Point out each leukocyte.
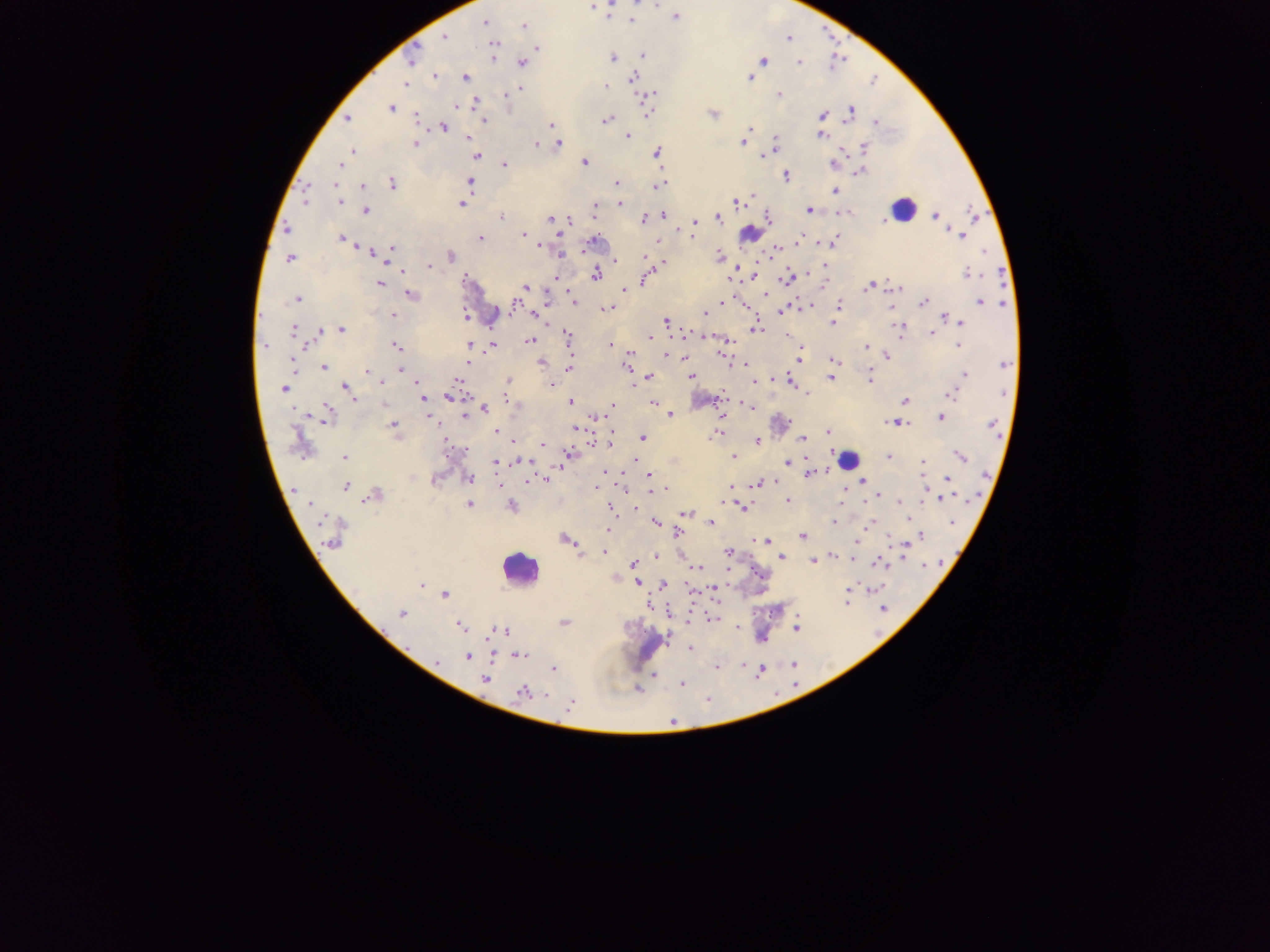

Approximate centers as (x, y) in pixels.
Leukocytes: (901, 210), (750, 233), (848, 460), (519, 568).

Summary:
  - Malaria parasite locations: (592, 5), (607, 15), (675, 16), (631, 19), (484, 22), (523, 26), (444, 37), (788, 37), (493, 44), (536, 49), (642, 55), (493, 58), (613, 58), (411, 59), (764, 60), (520, 62), (799, 62), (433, 76), (465, 76), (749, 77), (631, 79), (406, 83), (605, 86), (520, 89), (505, 93), (652, 93), (778, 93), (475, 99), (455, 106), (390, 107), (850, 110), (648, 113), (713, 113), (821, 116), (347, 118), (417, 118), (607, 119), (483, 120), (875, 122), (550, 125), (442, 126), (750, 128), (821, 135), (745, 136), (467, 137), (628, 137), (774, 140), (741, 142), (415, 143), (557, 143), (535, 144), (863, 148), (775, 149), (352, 150), (657, 153), (476, 156), (584, 161), (340, 164), (504, 164), (858, 172), (786, 175), (470, 181), (391, 182), (617, 184), (658, 184), (361, 186), (336, 188), (305, 190), (835, 190), (751, 194), (305, 198), (734, 200), (339, 201), (462, 203), (620, 204), (594, 208), (810, 209), (366, 210), (840, 211), (663, 215), (934, 215), (500, 216), (551, 218), (717, 218), (767, 218), (881, 218), (643, 219), (694, 222), (286, 228), (693, 230), (523, 234), (961, 235), (342, 238), (479, 238), (799, 239), (592, 241), (657, 241), (835, 241), (538, 246), (391, 247), (581, 250), (776, 250), (370, 251), (389, 253), (451, 255), (559, 255), (382, 256), (718, 256), (289, 258), (645, 258), (615, 259), (662, 262), (429, 265), (736, 266), (824, 266), (400, 271), (595, 273), (966, 274), (754, 276), (465, 278), (787, 278), (643, 280), (729, 281), (380, 283), (867, 286), (526, 287), (899, 288), (622, 289), (565, 290), (410, 295), (765, 295), (570, 296), (296, 299), (739, 300), (721, 302), (923, 302), (980, 302), (1002, 302), (573, 304), (743, 305), (838, 305), (891, 305), (512, 306), (802, 306), (810, 306), (606, 308), (782, 312), (702, 314), (392, 315), (467, 315), (535, 315), (462, 316), (943, 316), (834, 320), (665, 321), (960, 322), (832, 323), (753, 327), (898, 329), (294, 330), (340, 330), (319, 331), (931, 332), (686, 333), (567, 335), (648, 337), (726, 339), (531, 340), (470, 344), (475, 344), (610, 344), (956, 344), (492, 345), (263, 346), (395, 346), (866, 346), (798, 350), (629, 353), (722, 353), (665, 355), (886, 355), (684, 358), (798, 359), (832, 360), (291, 362), (466, 362), (541, 362), (744, 364), (323, 367), (401, 368), (569, 368), (367, 370), (964, 375), (649, 377), (691, 377), (830, 377), (773, 378), (868, 378), (457, 380), (508, 380), (790, 381), (382, 382), (632, 382), (752, 382), (416, 384), (506, 384), (551, 384), (346, 387), (284, 389), (805, 392), (950, 395), (451, 397), (352, 399), (427, 399), (719, 400), (904, 400), (424, 402), (570, 402), (742, 402), (385, 403), (654, 403), (746, 405), (612, 407), (484, 408), (326, 414), (671, 414), (428, 415), (464, 416), (597, 416), (941, 418), (890, 422), (899, 423), (392, 425), (575, 428), (495, 431), (828, 431), (714, 435), (805, 437), (642, 439), (444, 440), (803, 440), (512, 441), (610, 441), (591, 442), (755, 442), (299, 443), (543, 444), (462, 452), (888, 456), (960, 456), (345, 457), (733, 457), (565, 458), (636, 459), (520, 460), (787, 461), (496, 462), (922, 463), (606, 471), (809, 473), (648, 474), (467, 478), (856, 478), (947, 478), (862, 479), (435, 480), (545, 480), (648, 481), (774, 481), (757, 484), (344, 485), (498, 485), (731, 486), (844, 486), (596, 487), (651, 487), (924, 488), (664, 489), (659, 491), (374, 494), (878, 496), (942, 498), (788, 501), (899, 502), (469, 503), (924, 503), (840, 504), (311, 505), (512, 507), (608, 507), (741, 507), (686, 514), (908, 520), (711, 522), (833, 522), (872, 522), (655, 523), (949, 523), (868, 525), (608, 529), (677, 533), (802, 535), (920, 535), (332, 537), (566, 540), (766, 541), (855, 542), (899, 544), (905, 544), (728, 551), (604, 552), (833, 555), (656, 557), (853, 557), (781, 558), (903, 558), (812, 560), (881, 562), (633, 564), (924, 565), (698, 568), (614, 577), (637, 582), (422, 584), (662, 585), (714, 588), (870, 588), (847, 589), (444, 594), (847, 602), (647, 605), (884, 607), (401, 613), (669, 613), (711, 618), (688, 619), (564, 622), (459, 625), (796, 626), (737, 628), (499, 630), (689, 648), (518, 655), (468, 656), (435, 662), (742, 664), (717, 667), (553, 669), (654, 676), (484, 680), (681, 683), (638, 687), (522, 693), (544, 694), (570, 704)
  - Image size: 1270×952 pixels
  - Field of view: single
  - Capture: mobile-phone photograph through a microscope
  - Country: Ghana
  - Preparation: thick blood smear